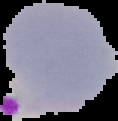

image_type: segmented cell region with the area outside set to black
preparation: thin blood smear
image_size: 118×121 pixels
result: Plasmodium parasites identified